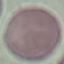

result: no malaria parasites detected
image_type: automatically extracted cell patch, resized to 64 × 64 pixels
capture: smartphone through the microscope eyepiece
preparation: thin blood film
stain: Giemsa